Identify the parasite.
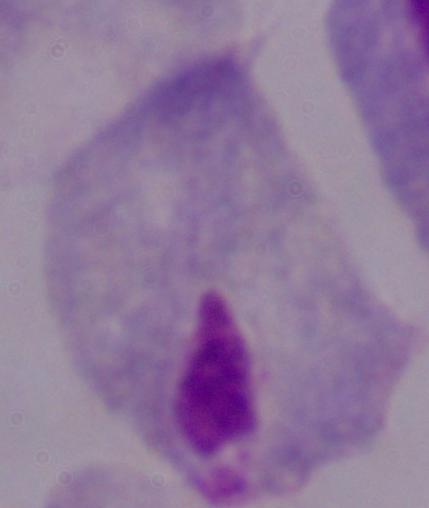
A trichomonad.

1000x magnification. Photomicrograph.